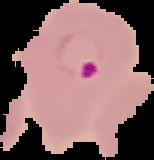
preparation: thin blood smear
image_type: segmented cell region with the area outside set to black
result: malaria parasites identified
image_size: 154×160 pixels